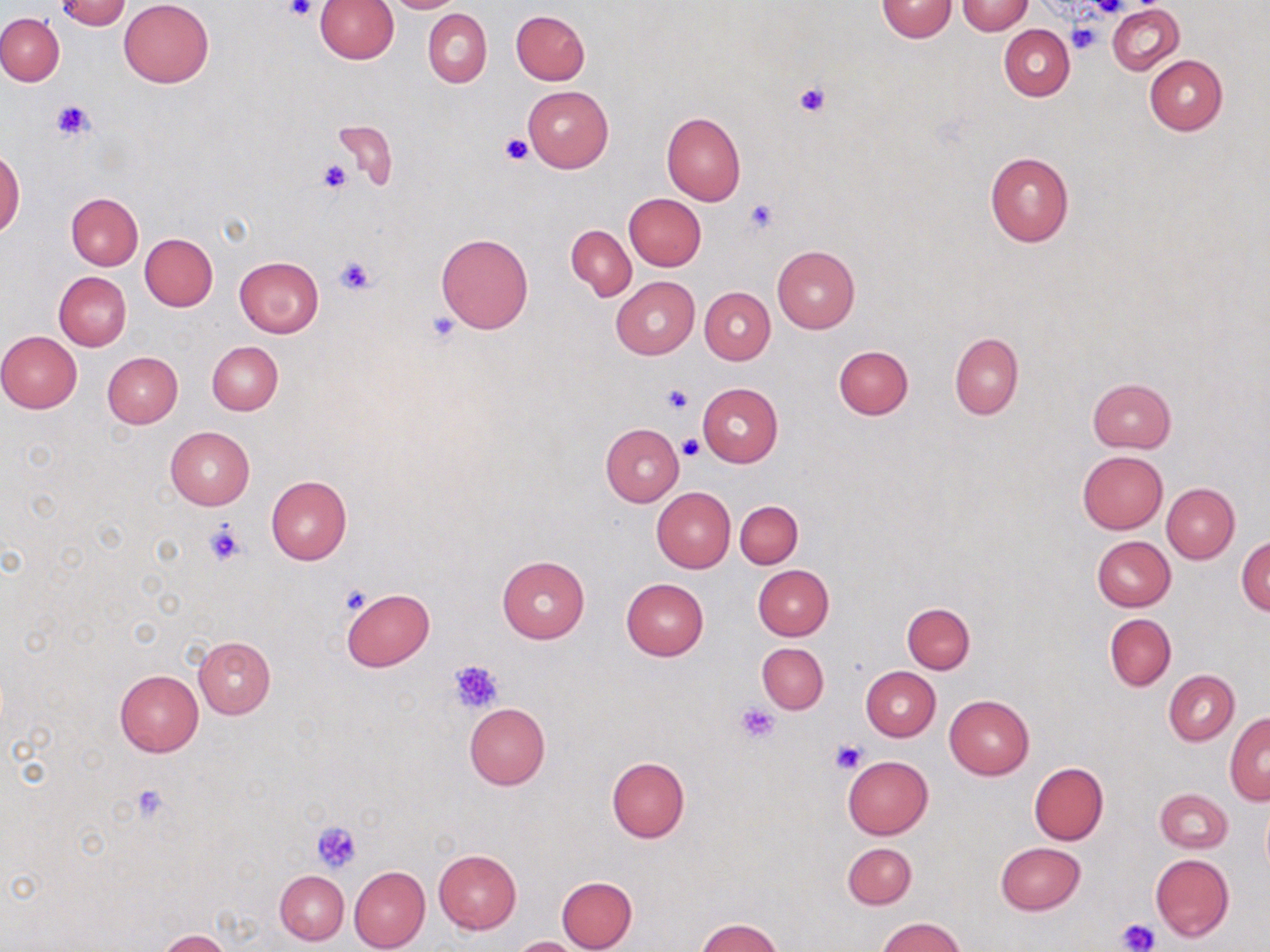
slide_level_diagnosis: no evidence of blood parasites
stain: May-Grünwald-Giemsa
field_of_view: single
uninfected_red_blood_cell_locations: 'approximate bounding boxes as (x1,y1)-(x2,y2) corner pairs in pixels: (55,0)-(132,30), (314,0)-(399,62), (386,0)-(463,12), (118,1)-(215,87), (877,1)-(956,41), (958,1)-(1034,34), (1108,3)-(1184,75), (423,9)-(492,87), (511,9)-(589,84), (0,14)-(65,86), (999,25)-(1075,100), (1145,55)-(1227,135), (523,86)-(613,173), (661,111)-(745,206), (333,122)-(396,188), (0,148)-(22,240), (985,152)-(1073,247), (67,193)-(143,270), (624,194)-(706,271), (566,226)-(636,300), (436,232)-(535,334), (140,233)-(218,310), (772,245)-(859,335), (234,256)-(325,338), (54,272)-(131,351), (610,277)-(699,359), (700,287)-(775,364), (0,331)-(82,413), (949,333)-(1024,419), (207,341)-(282,414), (834,345)-(913,419), (102,352)-(182,428), (1086,378)-(1175,453), (698,384)-(783,467), (600,424)-(683,505), (165,427)-(254,509), (1077,451)-(1168,535), (266,475)-(352,564), (1162,483)-(1240,564), (653,488)-(735,572), (735,501)-(802,567), (1091,536)-(1174,612), (1236,537)-(1270,616), (497,555)-(589,642), (752,564)-(834,641), (621,578)-(708,660), (341,588)-(434,671), (902,602)-(975,673), (1105,614)-(1175,691), (193,636)-(275,719), (757,643)-(828,713), (861,667)-(940,741), (114,669)-(203,756), (1164,670)-(1239,744), (944,694)-(1034,779), (464,703)-(550,789), (1225,713)-(1270,805), (842,755)-(933,840), (607,757)-(689,843), (1028,762)-(1108,845), (1155,788)-(1232,853), (1261,802)-(1270,877), (843,842)-(916,909), (995,842)-(1087,915), (434,849)-(521,934), (1151,854)-(1234,941), (348,865)-(430,952), (275,870)-(348,945), (556,876)-(638,952), (877,917)-(965,952), (695,918)-(785,952), (158,930)-(231,952), (509,936)-(585,952)'
modality: optical microscopy
preparation: thin blood smear
platelet_locations: 'approximate bounding boxes as (x1,y1)-(x2,y2) corner pairs in pixels: (284,0)-(317,22), (1084,0)-(1130,18), (1068,21)-(1102,55), (792,81)-(832,117), (50,99)-(96,143), (500,133)-(534,166), (317,159)-(354,194), (743,198)-(780,235), (334,256)-(375,295), (427,313)-(463,344), (661,385)-(695,415), (678,435)-(704,460), (203,521)-(248,567), (338,585)-(370,615), (449,659)-(504,714), (736,702)-(779,743), (832,740)-(866,773), (129,784)-(173,823), (312,821)-(361,872), (1117,918)-(1159,952)'
image_size: 1270×952 pixels
magnification: 1000x